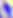
{
  "modality": "micrograph",
  "magnification": "400x",
  "identification": "Toxoplasma gondii"
}